Give the extent of all Plasmodium falciparum-infected red blood cells.
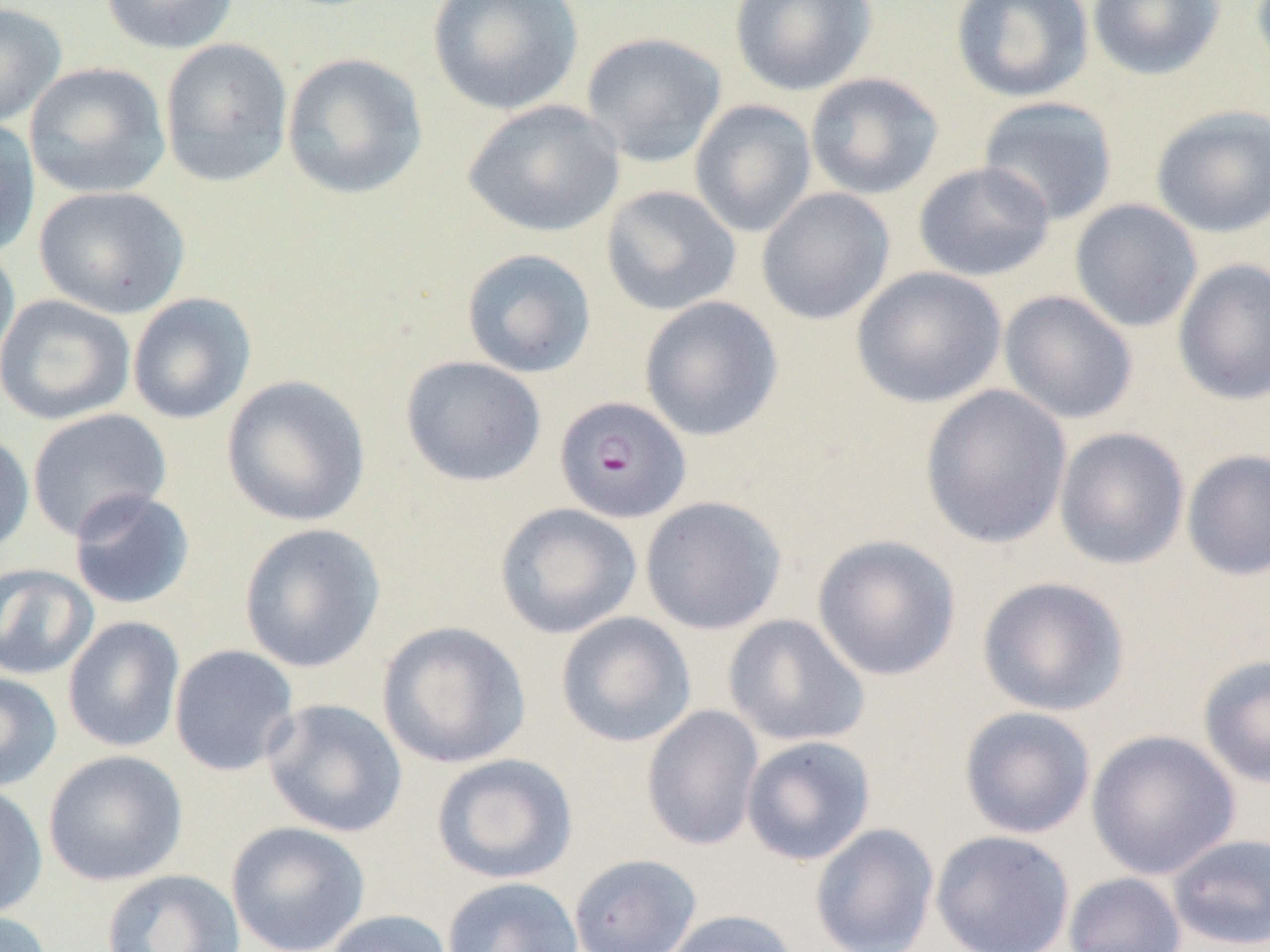
Approximate bounding boxes as (x1, y1, x2, y2) in pixels.
Plasmodium falciparum-infected red blood cells: (554, 395, 690, 523).

Uninfected red blood cell locations: (99, 0, 238, 55), (427, 0, 584, 116), (729, 0, 877, 96), (950, 0, 1094, 103), (1087, 0, 1224, 81), (0, 3, 67, 128), (581, 32, 728, 168), (159, 38, 293, 187), (281, 51, 428, 200), (25, 62, 171, 199), (805, 72, 944, 200), (977, 96, 1119, 226), (463, 99, 624, 238), (688, 100, 817, 238), (1151, 105, 1270, 238), (0, 117, 41, 259), (913, 161, 1055, 282), (600, 184, 741, 316), (33, 185, 190, 319), (756, 188, 895, 325), (1069, 199, 1203, 332), (0, 239, 20, 376), (460, 248, 596, 378), (1172, 258, 1270, 406), (851, 266, 1006, 408), (998, 290, 1138, 424), (127, 292, 257, 425), (0, 294, 136, 426), (638, 295, 783, 442), (400, 356, 546, 487), (221, 374, 371, 527), (919, 384, 1072, 550), (27, 408, 171, 541), (1053, 426, 1190, 571), (0, 431, 34, 558), (1181, 448, 1270, 581), (68, 488, 196, 610), (639, 495, 787, 635), (494, 503, 642, 639), (238, 522, 386, 673), (811, 534, 961, 681), (0, 563, 98, 680), (976, 576, 1131, 716), (556, 612, 696, 748), (722, 614, 870, 747), (62, 615, 186, 753), (376, 620, 531, 769), (168, 644, 300, 777), (1197, 653, 1270, 789), (0, 673, 62, 791), (262, 698, 407, 838), (641, 705, 764, 852), (958, 706, 1096, 839), (1086, 729, 1240, 880), (741, 735, 876, 866), (43, 749, 188, 887), (431, 753, 578, 885), (0, 783, 48, 919), (225, 821, 370, 952), (809, 823, 939, 952), (930, 830, 1075, 952), (1165, 832, 1270, 950), (568, 853, 702, 952), (100, 869, 245, 952), (1063, 872, 1186, 952), (442, 876, 583, 952), (321, 909, 453, 952), (660, 909, 801, 952), (0, 911, 54, 952). Slide-level diagnosis: Plasmodium falciparum. Thin blood smear. Image is 1270×952 pixels. One field of a larger specimen. Captured at 1000x magnification. Light microscopy.